Describe the morphology of the erythrocytes.
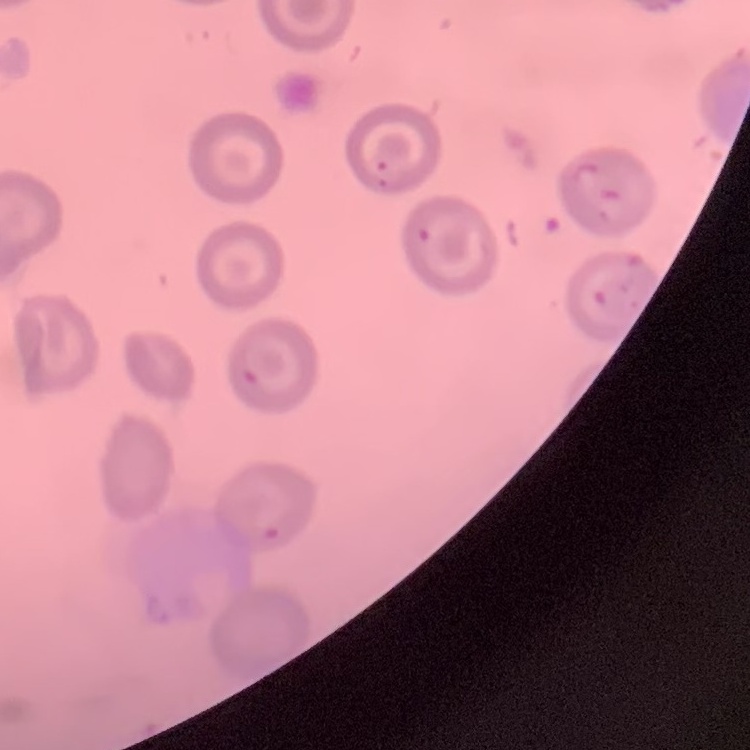
No rouleaux formation.

Field's or Giemsa stain. Thin blood film. Square crop of a larger photomicrograph.